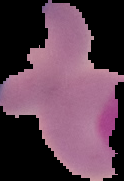
image size = 124×181 pixels
image type = segmented cell region with the area outside set to black
malaria status = uninfected
preparation = thin blood smear